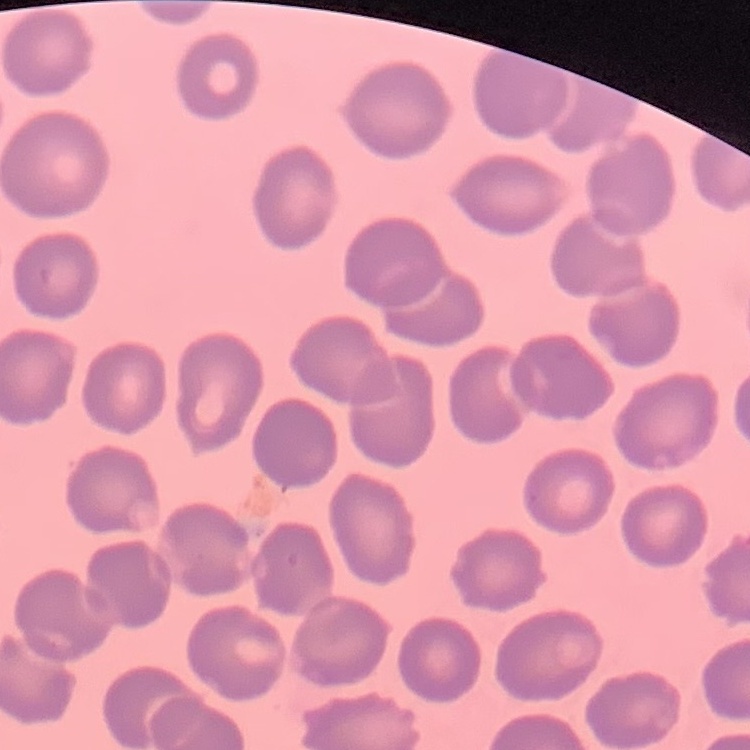 The red blood cells show no rouleaux formation. One tile cut from a larger photomicrograph. Field's or Giemsa stain. Thin peripheral smear.